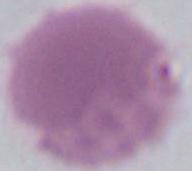
modality = micrograph
identification = erythrocyte
magnification = 1000x